Report the malaria status of this cell.
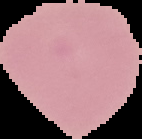
Uninfected.

{
  "image_size": "142×139 pixels",
  "image_type": "segmented cell region with the area outside set to black",
  "preparation": "thin blood smear"
}